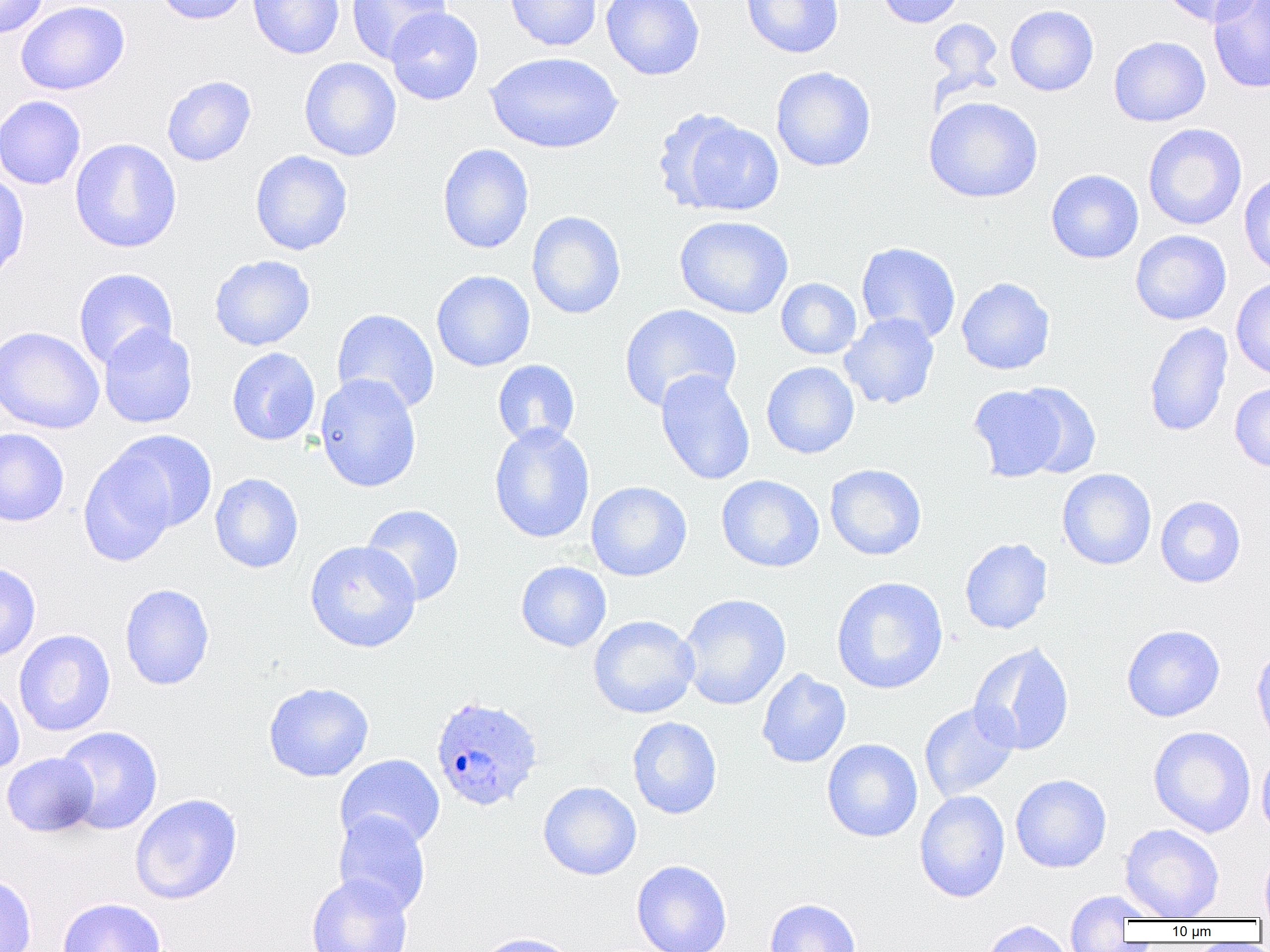

slide_level_diagnosis: Plasmodium ovale
modality: light microscopy
field_of_view: one of a larger specimen
magnification: 1000x
uninfected_red_blood_cell_locations: 'approximate bounding boxes as [x1, y1, x2, y2] in pixels: [0, 0, 49, 38], [16, 0, 130, 95], [154, 0, 253, 25], [248, 0, 345, 59], [346, 0, 450, 62], [505, 0, 603, 52], [601, 0, 705, 80], [740, 0, 844, 58], [874, 0, 967, 28], [1158, 0, 1263, 26], [1208, 1, 1270, 93], [1004, 4, 1099, 96], [385, 7, 483, 105], [927, 18, 1003, 90], [1108, 36, 1211, 126], [485, 51, 623, 154], [299, 57, 402, 161], [771, 66, 876, 172], [162, 75, 257, 166], [0, 95, 87, 190], [923, 96, 1043, 203], [655, 108, 783, 216], [1143, 123, 1247, 230], [69, 138, 182, 253], [437, 143, 534, 254], [250, 150, 353, 255], [1045, 169, 1144, 264], [0, 171, 30, 283], [1238, 173, 1270, 278], [527, 210, 626, 319], [674, 215, 794, 319], [1130, 230, 1232, 325], [855, 241, 961, 343], [209, 255, 316, 351], [74, 268, 177, 370], [431, 270, 535, 372], [956, 277, 1056, 375], [776, 278, 862, 359], [1231, 278, 1270, 380], [619, 304, 742, 412], [332, 308, 440, 415], [839, 312, 940, 410], [1144, 321, 1233, 438], [98, 325, 198, 428], [0, 326, 104, 434], [227, 347, 320, 446], [492, 359, 580, 448], [761, 361, 859, 459], [655, 369, 755, 486], [314, 373, 422, 493], [1230, 382, 1270, 472], [1013, 383, 1101, 479], [968, 384, 1070, 483], [489, 424, 595, 543], [0, 428, 70, 526], [108, 429, 218, 533], [78, 451, 178, 566], [825, 464, 927, 560], [1057, 468, 1157, 570], [210, 473, 303, 573], [717, 474, 825, 572], [586, 481, 692, 581], [1155, 496, 1246, 587], [360, 504, 465, 606], [960, 537, 1053, 635], [304, 540, 422, 653], [516, 561, 612, 652], [0, 562, 41, 662], [831, 576, 948, 694], [119, 583, 215, 690], [678, 594, 791, 710], [588, 615, 700, 719], [1122, 624, 1225, 722], [13, 629, 115, 737], [969, 642, 1075, 756], [1250, 643, 1270, 752], [757, 668, 851, 768], [0, 680, 25, 775], [263, 682, 374, 782], [919, 702, 1020, 803], [627, 716, 723, 819], [55, 725, 163, 835], [1148, 726, 1256, 837], [821, 739, 923, 842], [1256, 747, 1270, 843], [2, 752, 99, 837], [335, 754, 445, 851], [1011, 774, 1111, 873], [538, 781, 641, 880], [914, 791, 1010, 902], [130, 793, 242, 905], [332, 811, 431, 917], [1120, 823, 1224, 920], [1259, 845, 1270, 920], [631, 859, 732, 952], [0, 873, 37, 952], [306, 874, 413, 952], [1062, 890, 1153, 946], [57, 897, 167, 952], [765, 898, 861, 952], [980, 920, 1076, 952], [471, 931, 579, 952]'
image_size: 1270×952 pixels
preparation: thin blood smear
plasmodium_ovale_infected_red_blood_cell_locations: 'approximate bounding boxes as [x1, y1, x2, y2] in pixels: [430, 694, 544, 813]'